Locate every malaria parasite.
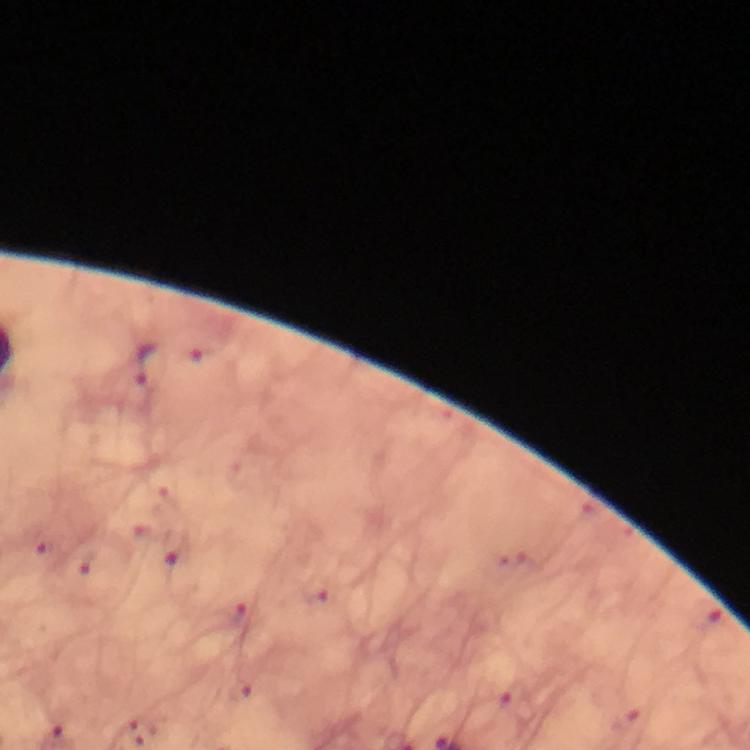
Approximate centers as {x, y} in pixels.
Malaria parasites: {199, 350}, {147, 365}, {38, 544}, {176, 548}, {84, 564}, {315, 590}, {235, 615}, {240, 691}, {512, 698}, {624, 720}, {137, 732}.

Summary:
  - Preparation: thick smear
  - Cropped from: one field of view
  - Image size: 750×750 pixels
  - Immersion oil: used
  - Magnification: 100x
  - Stain: Giemsa
  - Capture: smartphone photograph through a microscope
  - Context: from a diagnostic examination for malaria